Outline each Plasmodium falciparum parasite and classify it by life-cycle stage.
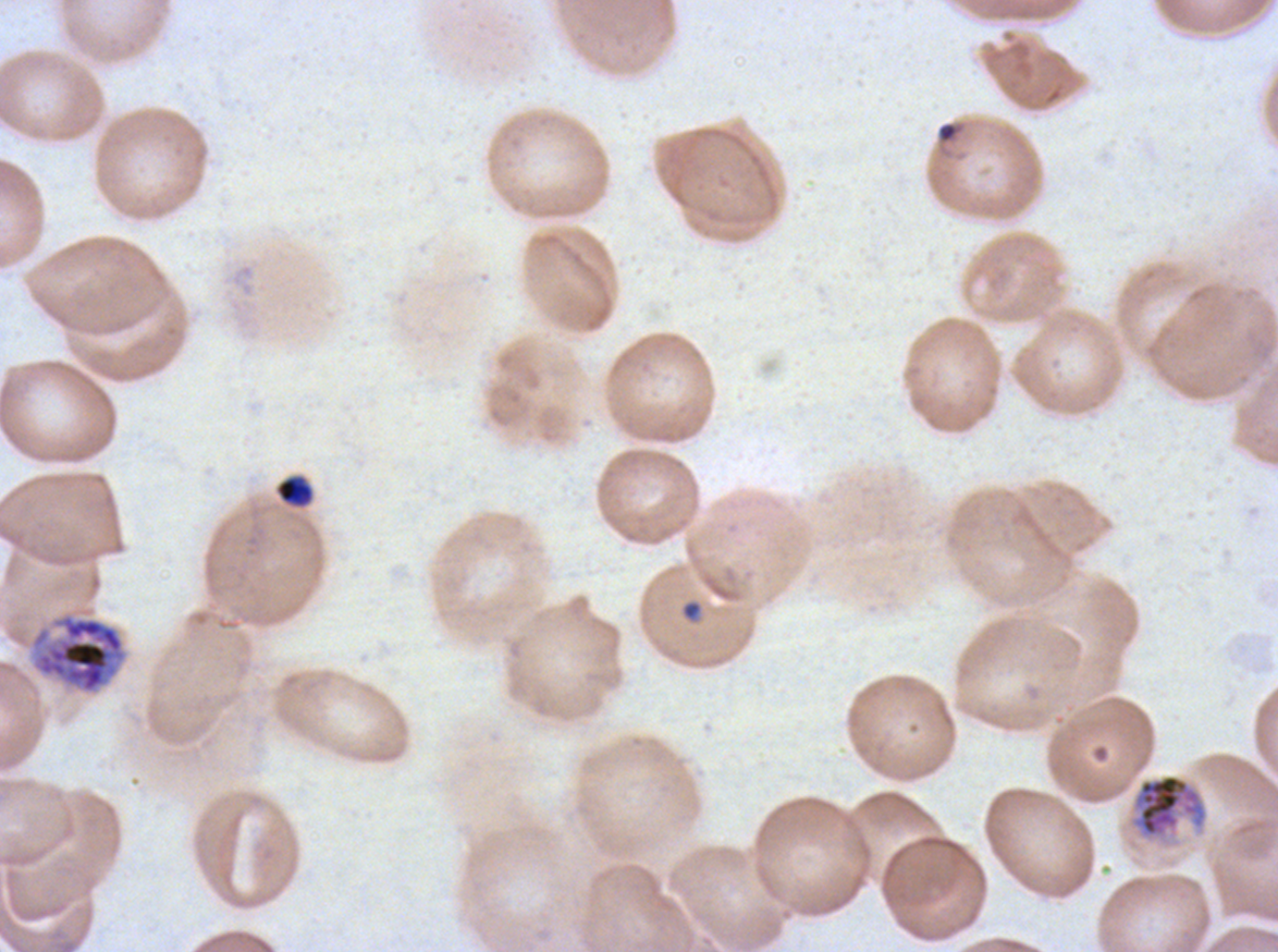

Approximate bounding boxes as [x1, y1, x2, y2] in pixels.
Rings: [938, 122, 958, 142], [680, 599, 703, 622].
Early schizonts: [28, 610, 129, 697], [1131, 773, 1208, 839].
No late-ring/early-trophozoite forms, mid trophozoites, late trophozoites, late schizonts, segmenters, or gametocytes observed.

{
  "specimen": "Plasmodium falciparum cultured ex vivo for 24 to 48 hours, from a patient in The Gambia",
  "life_cycle_stages_observed": "ring, early schizont",
  "image_size": "1278×952 pixels",
  "debris_locations": "approximate bounding boxes as [x1, y1, x2, y2] in pixels: [275, 475, 314, 507]",
  "field_of_view": "sub-image separated from a larger composite",
  "preparation": "thin blood smear",
  "stain": "Giemsa"
}